Identify the cell.
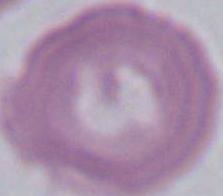

An erythrocyte.

Summary:
  - Modality: micrograph
  - Magnification: 1000x